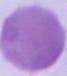

Summary:
  - Identification: erythrocyte
  - Modality: photomicrograph
  - Magnification: 1000x